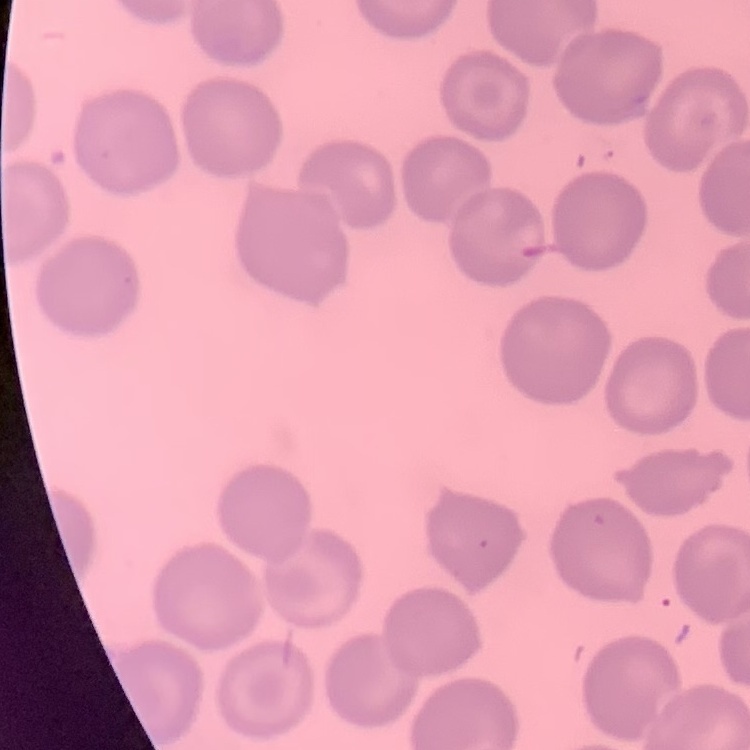

The red blood cells exhibit no rouleaux formation. One tile cut from a larger photomicrograph. Field's or Giemsa stain. Thin peripheral smear.